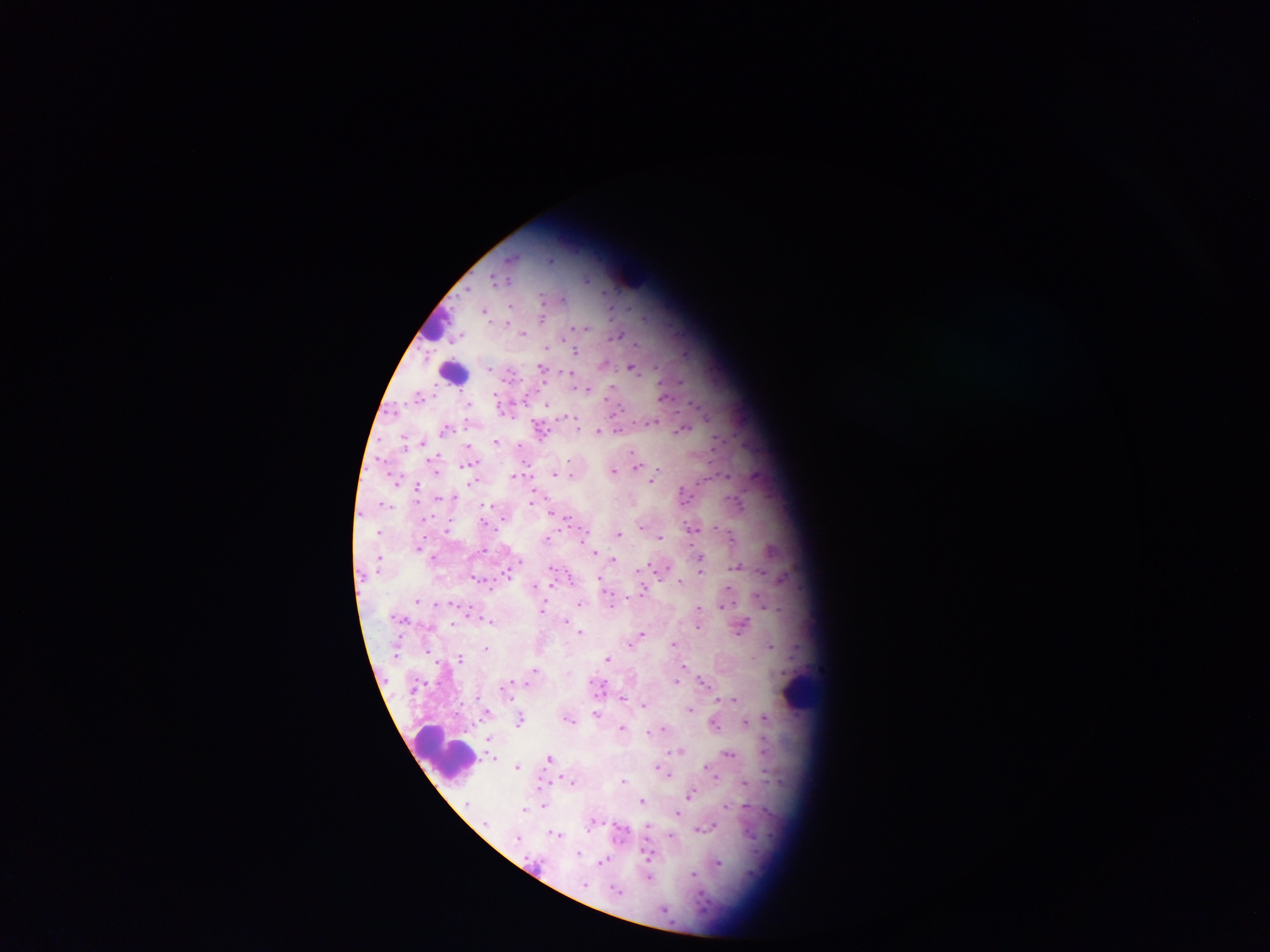

plasmodium_parasite_locations: 'approximate centers as {x, y} in pixels: {587, 281}, {511, 306}, {486, 315}, {543, 321}, {585, 330}, {524, 335}, {618, 337}, {636, 344}, {576, 352}, {631, 368}, {489, 369}, {541, 369}, {570, 375}, {613, 387}, {588, 390}, {661, 398}, {469, 406}, {547, 406}, {578, 431}, {681, 432}, {598, 434}, {498, 443}, {422, 445}, {468, 446}, {715, 446}, {632, 453}, {474, 463}, {637, 467}, {633, 469}, {614, 472}, {555, 476}, {514, 477}, {571, 477}, {727, 479}, {652, 481}, {397, 484}, {473, 484}, {416, 486}, {683, 497}, {440, 499}, {532, 504}, {740, 507}, {550, 514}, {567, 520}, {641, 528}, {692, 529}, {447, 532}, {380, 533}, {619, 535}, {660, 538}, {733, 538}, {548, 540}, {419, 550}, {485, 552}, {596, 554}, {702, 559}, {433, 560}, {614, 561}, {738, 568}, {641, 570}, {701, 571}, {762, 573}, {474, 578}, {601, 579}, {681, 583}, {644, 592}, {418, 602}, {451, 604}, {438, 605}, {580, 605}, {611, 605}, {724, 607}, {700, 609}, {542, 611}, {402, 620}, {488, 623}, {566, 623}, {453, 625}, {698, 628}, {742, 631}, {581, 634}, {642, 636}, {637, 640}, {675, 644}, {633, 647}, {770, 648}, {486, 650}, {428, 652}, {396, 655}, {461, 661}, {608, 661}, {683, 667}, {535, 671}, {704, 682}, {528, 683}, {678, 683}, {511, 684}, {507, 688}, {416, 689}, {599, 689}, {477, 699}, {624, 699}, {733, 701}, {644, 707}, {691, 712}, {487, 714}, {597, 716}, {765, 719}, {520, 722}, {570, 723}, {745, 723}, {715, 726}, {624, 729}, {664, 730}, {649, 733}, {489, 740}, {764, 750}, {680, 752}, {729, 755}, {494, 759}, {549, 759}, {517, 768}, {662, 771}, {669, 774}, {716, 780}, {544, 783}, {624, 783}, {745, 783}, {571, 784}, {691, 796}, {642, 802}, {467, 805}, {545, 805}, {746, 807}, {727, 808}, {525, 811}, {678, 815}, {486, 825}, {592, 825}, {648, 827}, {707, 829}, {622, 833}, {749, 835}, {557, 836}, {672, 838}, {517, 840}, {579, 854}, {648, 854}, {604, 862}, {538, 864}, {718, 865}, {694, 875}, {649, 878}, {586, 886}, {618, 893}, {665, 911}'
field_of_view: single
image_size: 1270×952 pixels
country: Ghana
preparation: thick blood smear
capture: mobile-phone photograph through a microscope
leukocyte_locations: 'approximate centers as {x, y} in pixels: {435, 326}, {453, 372}, {802, 692}, {445, 757}'